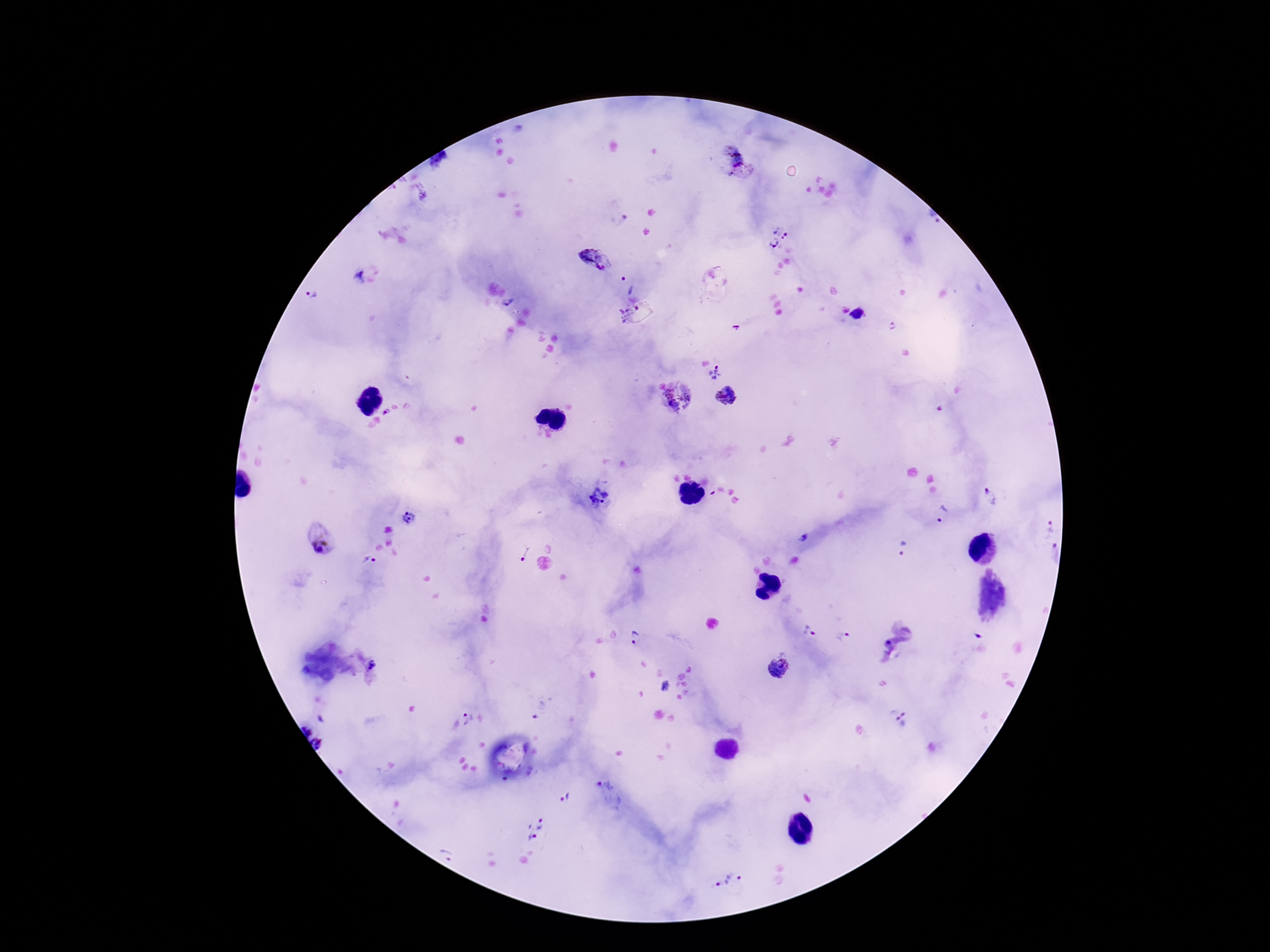
stain = Giemsa
field of view = single
image size = 1270×952 pixels
Plasmodium parasite locations = approximate object centers, in pixels from the top-left corner: (x=734, y=156), (x=932, y=218), (x=783, y=229), (x=773, y=244), (x=596, y=262), (x=358, y=277), (x=630, y=283), (x=312, y=295), (x=507, y=301), (x=626, y=308), (x=857, y=314), (x=715, y=372), (x=678, y=396), (x=727, y=396), (x=385, y=412), (x=989, y=496), (x=599, y=500), (x=941, y=516), (x=409, y=519), (x=1050, y=527), (x=804, y=538), (x=319, y=541), (x=902, y=547), (x=524, y=553), (x=1054, y=553), (x=370, y=560), (x=808, y=632), (x=842, y=637), (x=638, y=638), (x=888, y=642), (x=372, y=664), (x=775, y=667), (x=666, y=686), (x=539, y=710), (x=898, y=716), (x=468, y=718), (x=307, y=726), (x=323, y=742), (x=608, y=791), (x=565, y=799), (x=535, y=821), (x=532, y=837), (x=447, y=852), (x=726, y=880)
capture = smartphone camera through the microscope eyepiece
magnification = 100x
preparation = thick peripheral-blood smear
patient malaria status = positive